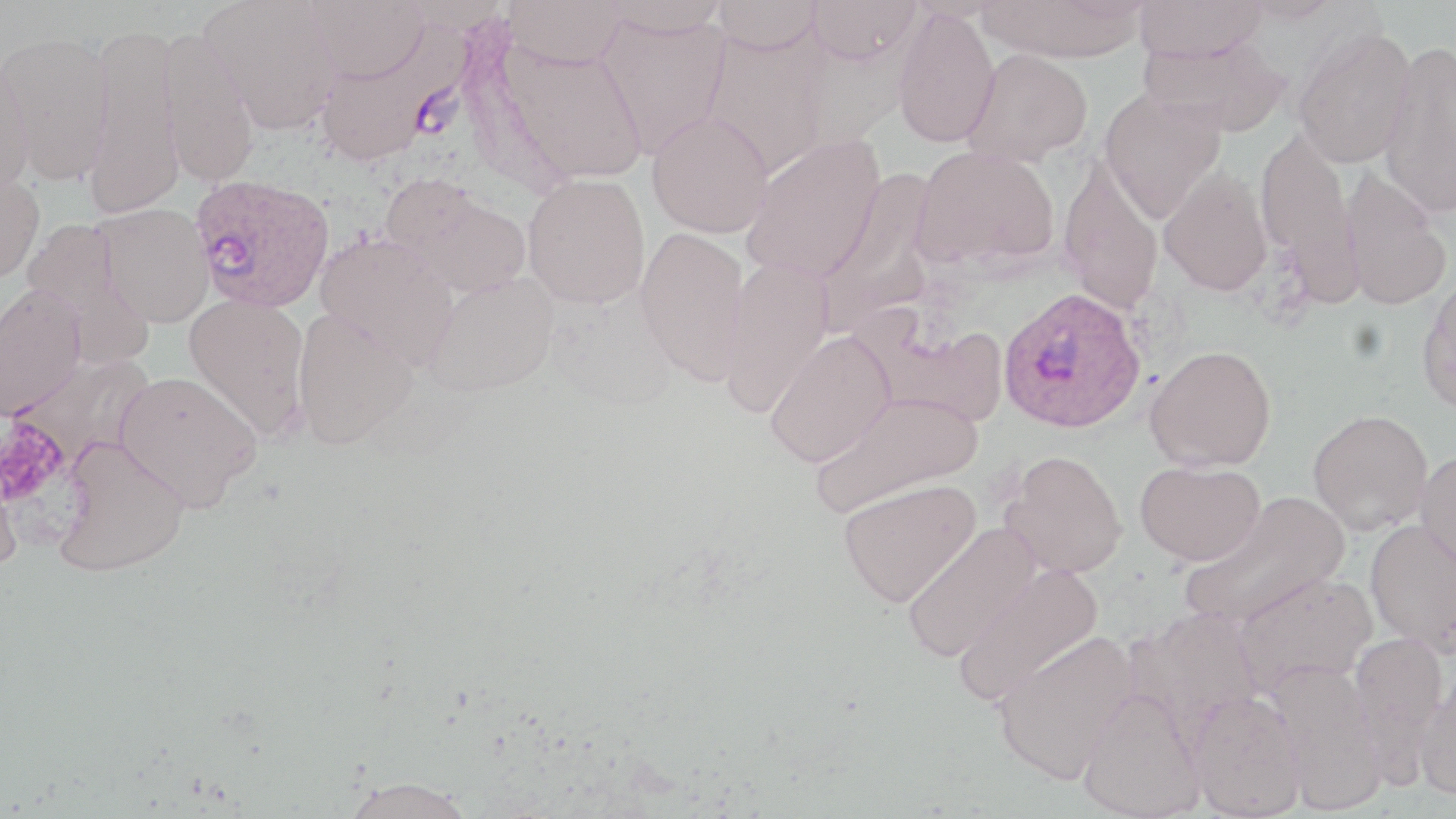
Summary:
  - Coordinate format: approximate bounding boxes as (x1,y1)-(x2,y2) corner pairs in pixels
  - Plasmodium ovale-infected red blood cell locations: (189,173)-(334,313), (997,285)-(1146,434)
  - Platelet locations: (0,416)-(73,510)
  - Uninfected red blood cell locations: (200,0)-(341,136), (504,0)-(628,69), (600,0)-(729,38), (712,0)-(822,53), (807,0)-(922,64), (979,0)-(1149,62), (1134,0)-(1267,62), (1237,0)-(1343,24), (305,1)-(431,84), (891,5)-(1001,148), (596,12)-(731,157), (82,22)-(183,219), (158,26)-(261,188), (313,26)-(458,168), (1293,26)-(1417,167), (702,30)-(829,177), (0,31)-(116,186), (1141,33)-(1291,137), (496,37)-(648,186), (1378,40)-(1456,220), (962,49)-(1092,168), (0,54)-(34,199), (1099,88)-(1226,222), (647,111)-(773,238), (1255,127)-(1357,288), (742,134)-(886,282), (913,145)-(1059,271), (1058,155)-(1164,316), (1158,168)-(1274,296), (0,170)-(45,285), (812,171)-(939,335), (1339,171)-(1451,311), (522,173)-(651,309), (384,175)-(532,299), (95,203)-(214,328), (20,217)-(153,367), (635,227)-(752,386), (315,231)-(459,370), (717,261)-(835,416), (424,273)-(558,397), (1416,275)-(1456,415), (0,284)-(87,420), (184,294)-(312,439), (292,307)-(418,449), (764,331)-(895,467), (1145,345)-(1276,472), (11,352)-(156,467), (114,370)-(262,511), (810,391)-(982,517), (1308,409)-(1434,535), (52,438)-(191,578), (1415,448)-(1456,577), (999,449)-(1128,577), (1135,460)-(1265,566), (0,465)-(23,577), (838,477)-(980,607), (1178,491)-(1352,630), (1365,519)-(1456,657), (902,524)-(1042,663), (953,563)-(1105,707), (1232,571)-(1376,697), (1123,607)-(1267,746), (992,630)-(1141,783), (1349,631)-(1448,776), (1268,661)-(1387,815), (1415,672)-(1456,800), (1077,687)-(1206,818), (1188,691)-(1307,819), (340,775)-(479,819)
  - Slide-level diagnosis: Plasmodium ovale
  - Stain: May-Grünwald-Giemsa
  - Modality: optical microscopy
  - Magnification: 1000x
  - Image size: 1456×819 pixels
  - Preparation: thin blood smear
  - Field of view: one of a larger specimen